Assess this cell for malaria.
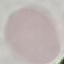
Uninfected.

Summary:
  - Preparation: thin blood smear
  - Capture: smartphone camera at the microscope eyepiece
  - Stain: Giemsa
  - Image type: cell patch, automatically extracted from a larger field of view and resized to 64 × 64 pixels